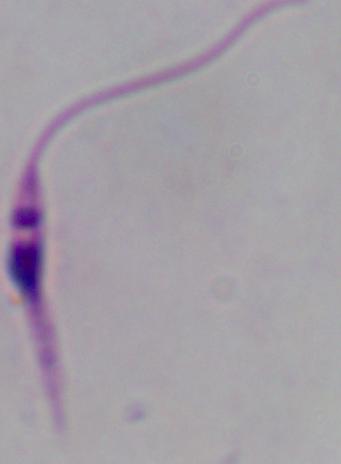
{
  "magnification": "1000x",
  "modality": "micrograph",
  "identification": "Leishmania"
}